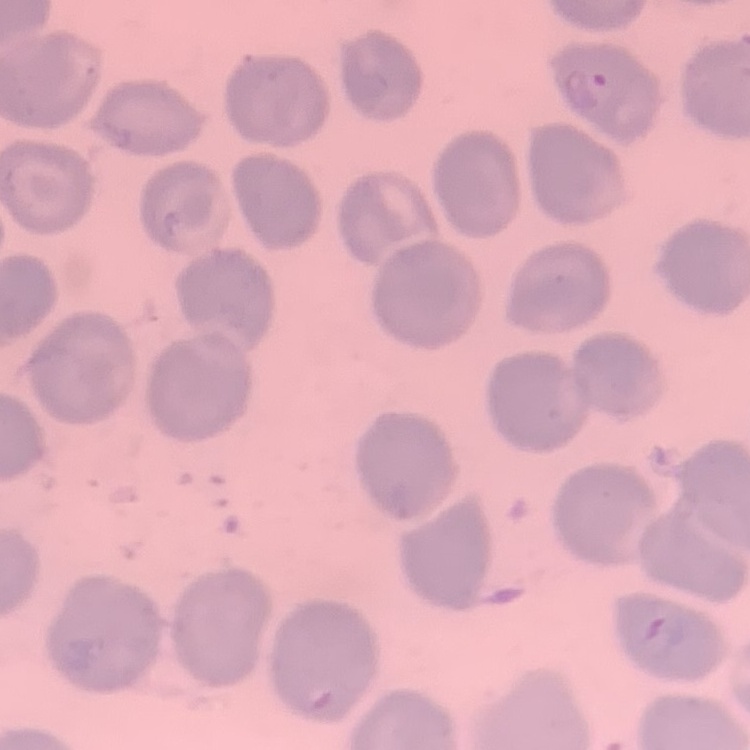

The red blood cells show no rouleaux formation. Square crop of a larger photomicrograph. Field's or Giemsa stain. Thin peripheral smear.